State which cell type is depicted.
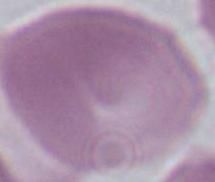

An erythrocyte.

Micrograph. Captured at 1000x magnification.